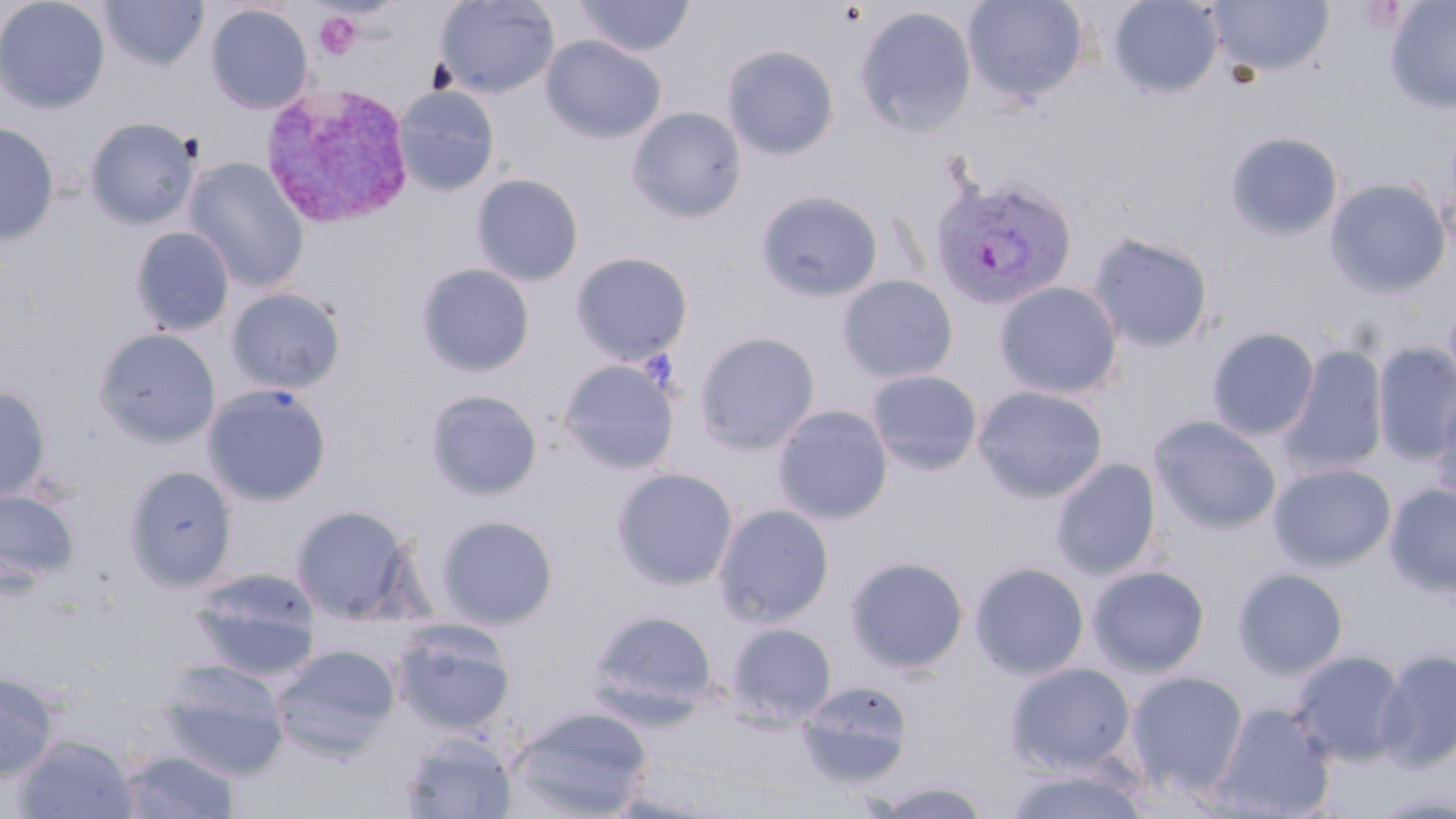

Summary:
  - Coordinate format: approximate bounding boxes as named x1/y1/x2/y2 corners in pixels
  - Uninfected red blood cell locations: (x1=0, y1=0, x2=111, y2=114), (x1=99, y1=0, x2=209, y2=71), (x1=434, y1=0, x2=560, y2=99), (x1=574, y1=0, x2=695, y2=58), (x1=963, y1=0, x2=1088, y2=103), (x1=1107, y1=0, x2=1223, y2=99), (x1=1206, y1=0, x2=1334, y2=78), (x1=1385, y1=0, x2=1456, y2=113), (x1=205, y1=4, x2=313, y2=114), (x1=855, y1=6, x2=977, y2=138), (x1=540, y1=35, x2=666, y2=143), (x1=722, y1=44, x2=840, y2=160), (x1=393, y1=85, x2=500, y2=196), (x1=627, y1=106, x2=746, y2=223), (x1=85, y1=116, x2=200, y2=230), (x1=0, y1=122, x2=59, y2=246), (x1=1225, y1=131, x2=1344, y2=241), (x1=183, y1=157, x2=309, y2=293), (x1=471, y1=173, x2=585, y2=286), (x1=1325, y1=179, x2=1450, y2=297), (x1=755, y1=189, x2=883, y2=303), (x1=131, y1=227, x2=234, y2=335), (x1=1088, y1=232, x2=1214, y2=353), (x1=570, y1=251, x2=694, y2=364), (x1=415, y1=263, x2=535, y2=377), (x1=837, y1=274, x2=958, y2=383), (x1=994, y1=282, x2=1123, y2=399), (x1=226, y1=287, x2=346, y2=394), (x1=1443, y1=298, x2=1456, y2=396), (x1=93, y1=327, x2=221, y2=448), (x1=1206, y1=327, x2=1320, y2=441), (x1=694, y1=331, x2=820, y2=454), (x1=1372, y1=342, x2=1456, y2=465), (x1=1277, y1=344, x2=1388, y2=478), (x1=558, y1=359, x2=680, y2=473), (x1=865, y1=369, x2=983, y2=476), (x1=202, y1=383, x2=333, y2=506), (x1=0, y1=385, x2=52, y2=505), (x1=972, y1=385, x2=1108, y2=502), (x1=425, y1=388, x2=544, y2=501), (x1=1429, y1=391, x2=1456, y2=515), (x1=772, y1=404, x2=893, y2=524), (x1=1149, y1=415, x2=1282, y2=535), (x1=1050, y1=457, x2=1162, y2=580), (x1=1268, y1=462, x2=1396, y2=570), (x1=123, y1=464, x2=238, y2=591), (x1=611, y1=467, x2=739, y2=590), (x1=1384, y1=482, x2=1456, y2=597), (x1=0, y1=489, x2=79, y2=587), (x1=290, y1=503, x2=418, y2=624), (x1=713, y1=503, x2=835, y2=627), (x1=435, y1=514, x2=559, y2=629), (x1=845, y1=555, x2=969, y2=674), (x1=970, y1=561, x2=1090, y2=680), (x1=1087, y1=565, x2=1210, y2=676), (x1=188, y1=566, x2=321, y2=678), (x1=1232, y1=567, x2=1349, y2=679), (x1=587, y1=610, x2=718, y2=721), (x1=390, y1=622, x2=516, y2=736), (x1=725, y1=622, x2=837, y2=726), (x1=271, y1=645, x2=401, y2=759), (x1=1374, y1=648, x2=1456, y2=772), (x1=1289, y1=649, x2=1411, y2=766), (x1=157, y1=660, x2=290, y2=779), (x1=1004, y1=661, x2=1136, y2=775), (x1=1125, y1=670, x2=1249, y2=795), (x1=0, y1=672, x2=58, y2=781), (x1=796, y1=679, x2=915, y2=789), (x1=1211, y1=702, x2=1335, y2=818), (x1=509, y1=706, x2=653, y2=818), (x1=14, y1=733, x2=138, y2=818), (x1=398, y1=733, x2=519, y2=818), (x1=118, y1=749, x2=242, y2=818), (x1=1001, y1=764, x2=1153, y2=819), (x1=871, y1=780, x2=994, y2=818), (x1=1367, y1=789, x2=1456, y2=818)
  - Plasmodium vivax-infected red blood cell locations: (x1=258, y1=81, x2=415, y2=230), (x1=930, y1=172, x2=1079, y2=310)
  - Platelet locations: (x1=314, y1=11, x2=361, y2=59)
  - Slide-level diagnosis: Plasmodium vivax
  - Field of view: single
  - Magnification: 1000x
  - Modality: optical microscopy
  - Preparation: thin blood smear
  - Stain: May-Grünwald-Giemsa
  - Image size: 1456×819 pixels